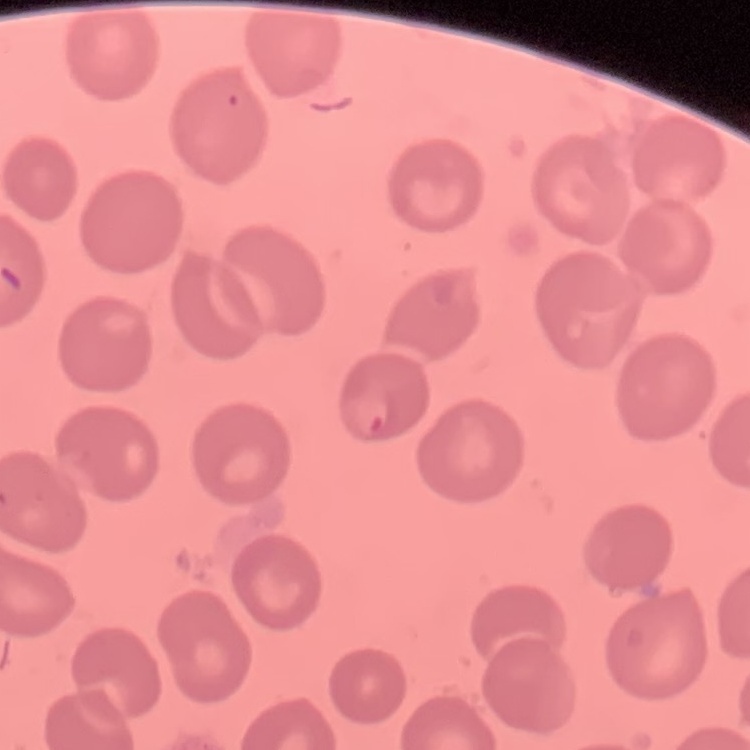
The red blood cells exhibit no rouleaux formation. Field's or Giemsa stain. Thin peripheral smear. Square crop of a larger photomicrograph.